Find the red blood cells that are infected with P. falciparum, and any of indeterminate infection status.
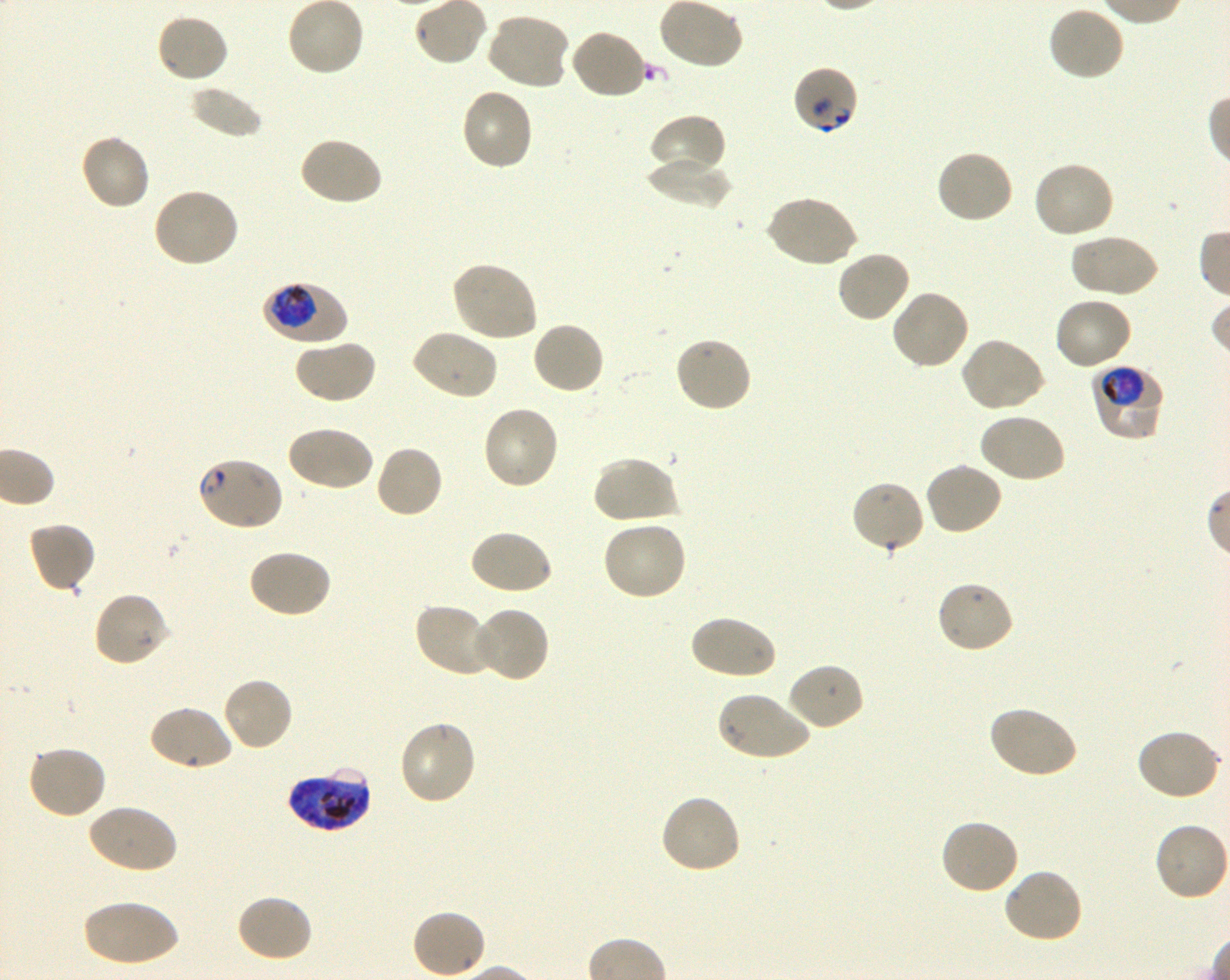

Approximate bounding rectangles given as corner coordinates in pixels from the top-left. Not every red blood cell is marked. A life-cycle stage — or a range of stages, where the recorded stages span more than one — follows each staged infected red blood cell.
Infected red blood cells: (x1=263, y1=281, x2=348, y2=345) early trophozoite to early schizont; (x1=1091, y1=363, x2=1165, y2=440) trophozoite; (x1=286, y1=767, x2=371, y2=832) late trophozoite to late schizont.
Red blood cells of indeterminate infection status: (x1=792, y1=67, x2=860, y2=135), (x1=194, y1=456, x2=284, y2=532).

Locations of uninfected red blood cells: (x1=286, y1=0, x2=365, y2=78), (x1=1047, y1=5, x2=1126, y2=82), (x1=484, y1=12, x2=571, y2=91), (x1=155, y1=13, x2=230, y2=84), (x1=567, y1=28, x2=648, y2=101), (x1=189, y1=85, x2=263, y2=138), (x1=459, y1=87, x2=534, y2=172), (x1=648, y1=114, x2=728, y2=182), (x1=78, y1=132, x2=151, y2=212), (x1=298, y1=135, x2=383, y2=207), (x1=935, y1=148, x2=1015, y2=226), (x1=645, y1=155, x2=731, y2=209), (x1=1031, y1=160, x2=1115, y2=240), (x1=152, y1=188, x2=240, y2=269), (x1=766, y1=194, x2=859, y2=268), (x1=1068, y1=233, x2=1159, y2=299), (x1=836, y1=249, x2=911, y2=324), (x1=449, y1=260, x2=539, y2=343), (x1=890, y1=287, x2=970, y2=371), (x1=1053, y1=296, x2=1133, y2=371), (x1=530, y1=320, x2=606, y2=395), (x1=409, y1=328, x2=498, y2=402), (x1=674, y1=337, x2=753, y2=414), (x1=959, y1=337, x2=1048, y2=414), (x1=294, y1=338, x2=378, y2=404), (x1=481, y1=404, x2=561, y2=491), (x1=977, y1=412, x2=1066, y2=484), (x1=284, y1=424, x2=374, y2=492), (x1=374, y1=444, x2=444, y2=520), (x1=591, y1=455, x2=678, y2=526), (x1=923, y1=462, x2=1004, y2=536), (x1=849, y1=479, x2=925, y2=555), (x1=27, y1=520, x2=97, y2=594), (x1=600, y1=520, x2=688, y2=602), (x1=468, y1=528, x2=554, y2=596), (x1=246, y1=548, x2=332, y2=619), (x1=935, y1=579, x2=1015, y2=655), (x1=93, y1=591, x2=171, y2=669), (x1=413, y1=602, x2=495, y2=678), (x1=472, y1=606, x2=551, y2=684), (x1=688, y1=614, x2=777, y2=681), (x1=786, y1=662, x2=866, y2=732), (x1=222, y1=676, x2=295, y2=751), (x1=716, y1=690, x2=811, y2=763), (x1=147, y1=704, x2=234, y2=773), (x1=989, y1=705, x2=1080, y2=779), (x1=397, y1=719, x2=477, y2=807), (x1=1135, y1=728, x2=1223, y2=802), (x1=26, y1=743, x2=107, y2=820), (x1=660, y1=793, x2=743, y2=875), (x1=87, y1=803, x2=178, y2=875), (x1=939, y1=818, x2=1021, y2=896), (x1=1154, y1=821, x2=1230, y2=903), (x1=1002, y1=867, x2=1085, y2=944), (x1=234, y1=893, x2=314, y2=963), (x1=81, y1=898, x2=179, y2=967), (x1=410, y1=909, x2=487, y2=979). Blood group of the donor: O+. Single field of view. 100x oil-immersion objective, numerical aperture 1.30. Thin blood smear. P. falciparum strain 3D7 in shaking in-vitro culture. Giemsa-stained preparation. Image is 1230×980 pixels.